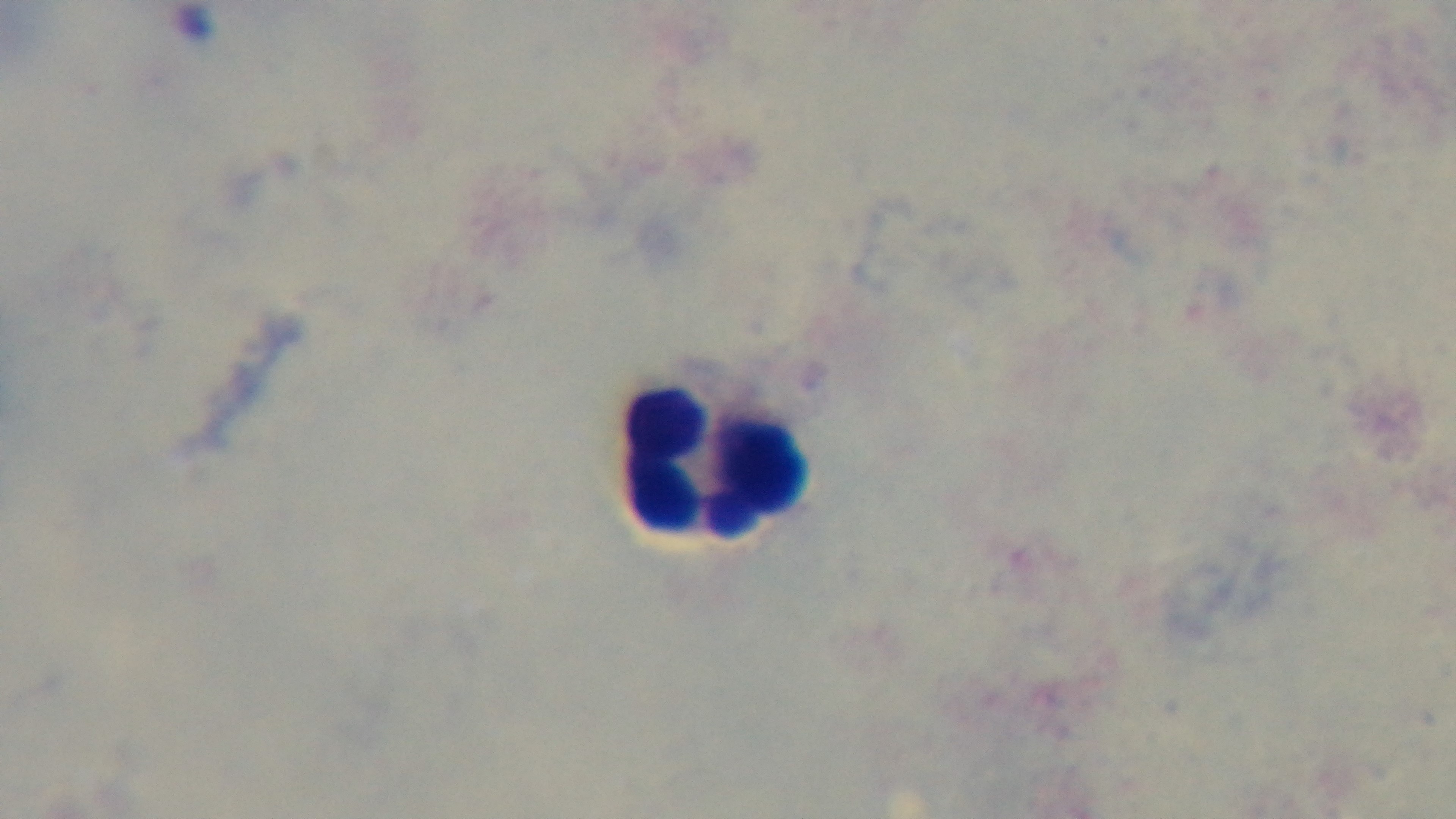
field_of_view: single
preparation: thick
malaria_status: uninfected
objective: 100x oil immersion
stain: Giemsa
modality: light microscopy
capture: mounted 4K digital camera